Identify the cell.
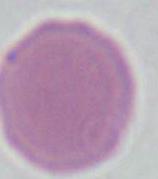

This is an erythrocyte.

Photomicrograph. Captured at 1000x magnification.